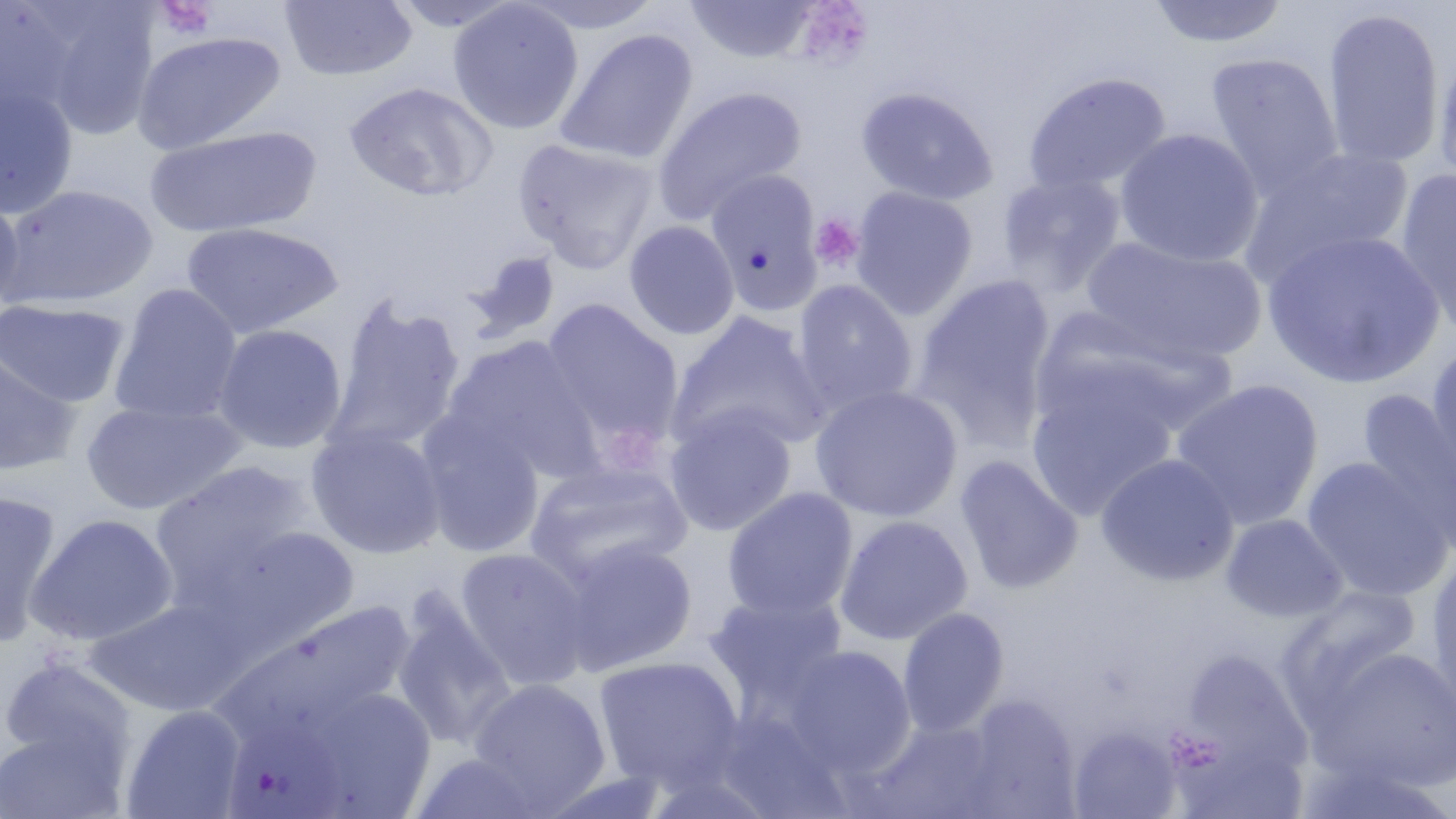
Summary:
  - Coordinate format: approximate bounding boxes as (x1,y1)-(x2,y2) corner pairs in pixels
  - Platelet locations: (156,0)-(217,40), (809,213)-(865,272)
  - Uninfected red blood cell locations: (279,0)-(417,81), (386,0)-(523,32), (447,0)-(584,135), (517,0)-(664,34), (685,0)-(821,63), (1148,0)-(1290,48), (1,1)-(86,127), (33,5)-(160,140), (1321,7)-(1445,171), (554,28)-(699,166), (132,30)-(286,154), (1432,46)-(1456,192), (1205,52)-(1343,197), (1022,72)-(1173,194), (344,81)-(497,202), (651,85)-(806,224), (1,86)-(78,217), (856,87)-(998,206), (144,125)-(322,239), (1114,127)-(1265,267), (512,138)-(659,273), (1239,145)-(1416,284), (704,168)-(824,313), (1393,169)-(1456,339), (996,173)-(1127,296), (3,184)-(157,309), (850,186)-(977,320), (0,195)-(25,315), (624,220)-(740,340), (180,222)-(343,338), (1262,228)-(1445,390), (1082,235)-(1266,366), (463,251)-(561,344), (910,275)-(1057,451), (792,279)-(918,415), (108,283)-(243,426), (324,295)-(466,456), (0,298)-(130,409), (540,299)-(684,452), (1037,306)-(1244,443), (666,312)-(831,455), (212,323)-(348,454), (443,336)-(604,481), (1425,343)-(1456,488), (0,349)-(83,477), (1025,366)-(1180,519), (1169,378)-(1325,529), (810,384)-(964,523), (1359,389)-(1456,546), (80,400)-(245,515), (665,405)-(798,537), (416,411)-(547,557), (306,425)-(448,559), (1095,452)-(1240,587), (954,455)-(1083,595), (1301,456)-(1454,601), (150,461)-(317,605), (524,461)-(692,590), (722,487)-(859,621), (0,490)-(63,647), (24,513)-(179,647), (1221,514)-(1348,623), (834,515)-(974,646), (197,523)-(363,653), (556,539)-(698,676), (454,546)-(595,690), (1425,552)-(1456,711), (1277,585)-(1423,724), (704,591)-(847,717), (391,597)-(517,753), (87,599)-(245,716), (211,600)-(418,754), (898,606)-(1010,736), (1182,633)-(1315,784), (782,645)-(917,776), (1310,646)-(1456,791), (0,656)-(136,772), (592,656)-(745,791), (468,677)-(612,814), (276,686)-(440,819), (957,694)-(1080,816), (120,704)-(248,818), (708,709)-(851,817), (867,718)-(1006,817), (0,724)-(130,819), (1068,725)-(1182,818), (406,751)-(554,819)
  - Slide-level diagnosis: no evidence of blood parasites
  - Preparation: thin blood film
  - Modality: light microscopy
  - Image size: 1456×819 pixels
  - Field of view: single
  - Stain: May-Grünwald-Giemsa
  - Magnification: 1000x